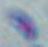

Summary:
  - Magnification: 1000x
  - Modality: micrograph
  - Identification: Toxoplasma gondii